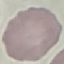 Result: negative for malaria parasites. Giemsa stain. Thin smear of blood. Acquired by smartphone through the microscope eyepiece. Automatically extracted cell patch, resized to 64 × 64 pixels.